Point out each leukocyte.
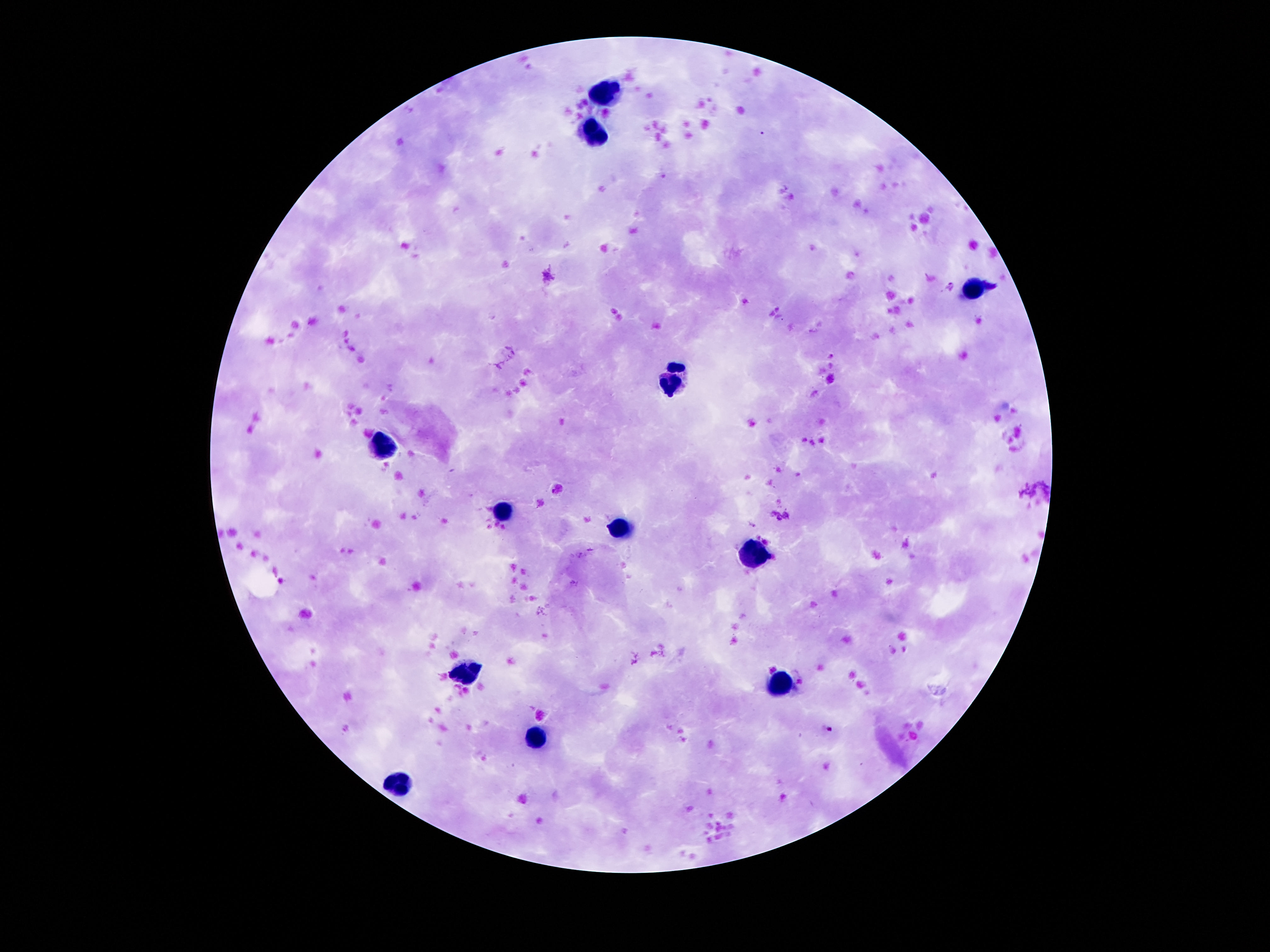

Approximate object centers, in pixels from the top-left corner.
Leukocytes: (x=607, y=93), (x=592, y=129), (x=973, y=289), (x=671, y=379), (x=383, y=448), (x=503, y=510), (x=622, y=525), (x=755, y=558), (x=462, y=674), (x=779, y=685), (x=534, y=736), (x=398, y=786).

Summary:
  - Image size: 1270×952 pixels
  - Patient malaria status: uninfected
  - Magnification: 100x
  - Field of view: one from this slide
  - Preparation: thick blood film
  - Capture: smartphone camera through the microscope eyepiece
  - Stain: Giemsa